Give the position of every malaria parasite.
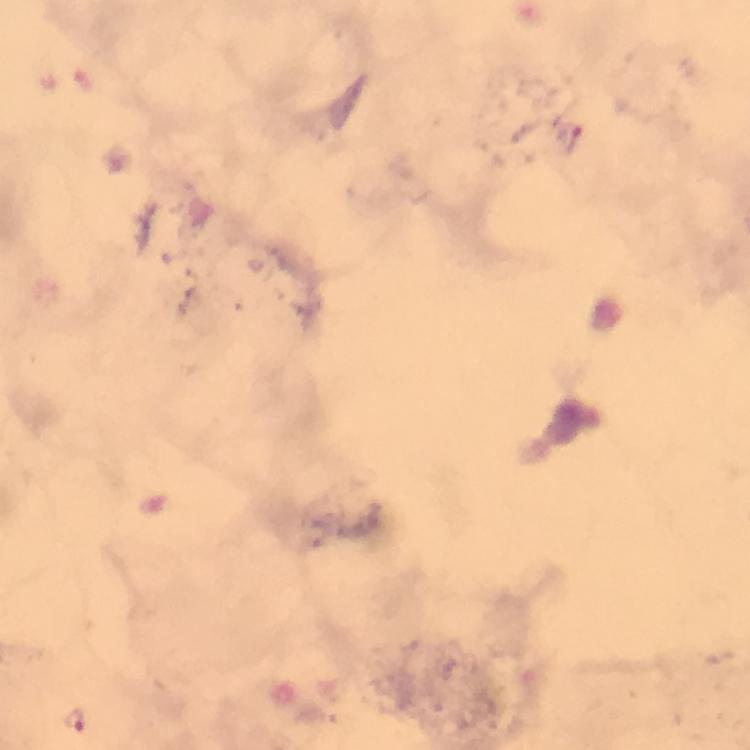

Approximate centers as [x, y] in pixels.
Malaria parasites: [570, 139], [75, 718].

From a malaria diagnostic workup. Thick smear. Immersion oil was used. Image is 750×750 pixels. Cropped region of a single field of view. At 100x magnification. Giemsa-stained preparation. Photographed with a smartphone mounted on the microscope.